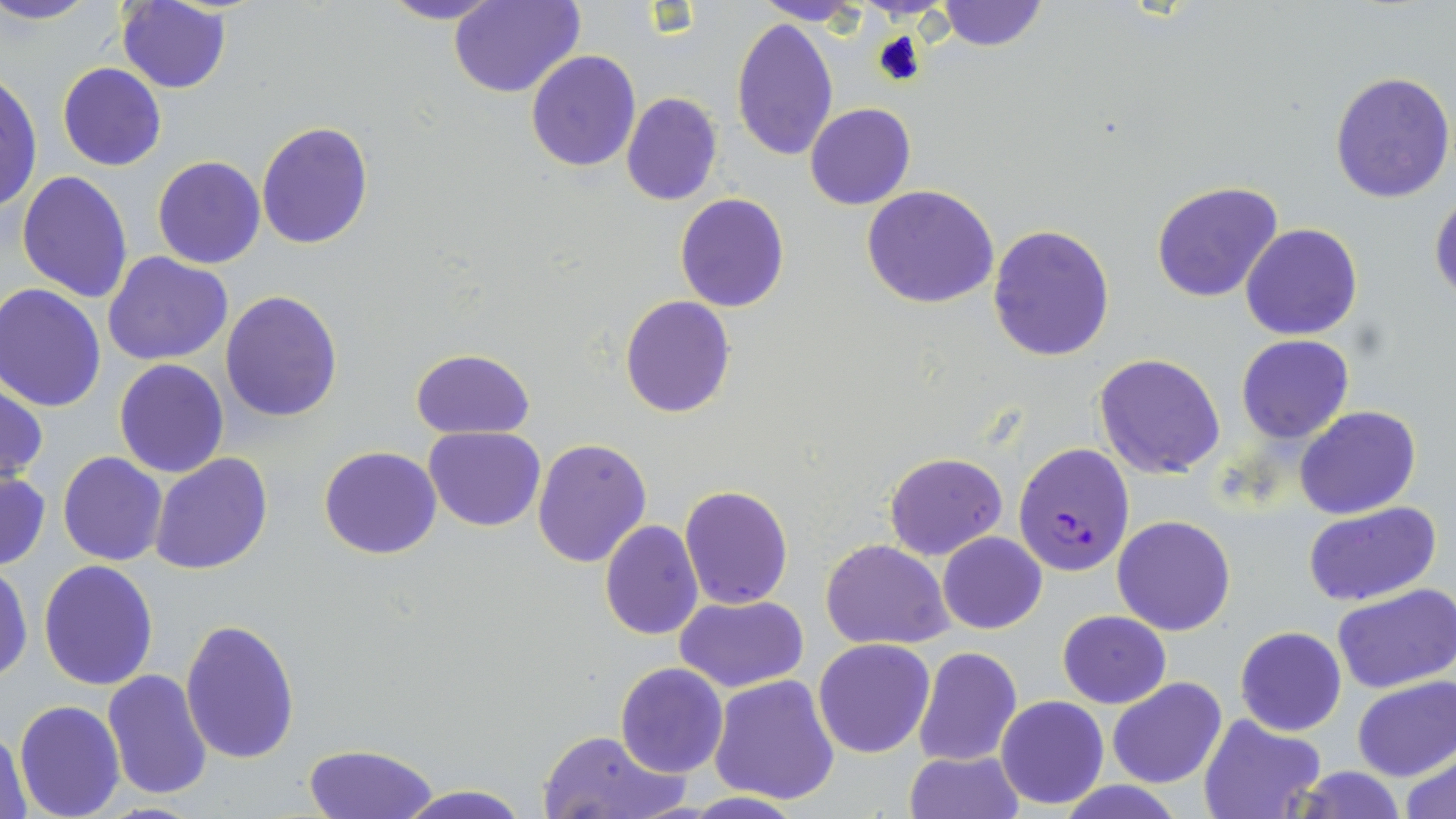

{
  "slide_level_diagnosis": "Plasmodium falciparum",
  "magnification": "1000x",
  "uninfected_red_blood_cell_locations": "approximate bounding boxes as (x1,y1)-(x2,y2) corner pairs in pixels: (0,0)-(102,26), (378,0)-(510,25), (754,0)-(867,26), (935,0)-(1048,52), (117,1)-(232,94), (448,1)-(584,99), (731,16)-(840,161), (526,48)-(640,172), (56,62)-(167,171), (1330,70)-(1455,204), (0,72)-(42,216), (620,93)-(723,206), (804,103)-(916,210), (256,121)-(374,249), (153,155)-(266,269), (17,169)-(133,304), (1151,179)-(1283,304), (861,184)-(1000,309), (1429,188)-(1456,302), (675,192)-(789,311), (1241,223)-(1363,340), (987,224)-(1115,363), (104,252)-(233,365), (0,285)-(107,411), (221,291)-(343,423), (620,296)-(735,419), (1236,334)-(1354,444), (410,347)-(534,440), (1093,353)-(1226,477), (114,359)-(229,477), (0,382)-(46,489), (1293,406)-(1421,519), (424,426)-(545,530), (532,439)-(652,569), (319,445)-(442,560), (58,451)-(167,566), (883,451)-(1007,560), (151,453)-(272,575), (0,471)-(50,570), (679,484)-(794,610), (1303,501)-(1442,604), (1112,515)-(1236,635), (598,518)-(704,640), (938,532)-(1046,634), (821,538)-(953,650), (0,556)-(33,684), (39,560)-(159,690), (1331,584)-(1456,694), (675,594)-(808,691), (1058,609)-(1171,709), (182,619)-(301,764), (1235,626)-(1347,736), (812,638)-(936,759), (914,647)-(1021,766), (615,662)-(729,778), (102,670)-(212,798), (709,674)-(841,806), (1107,676)-(1228,789), (1353,677)-(1455,782), (995,695)-(1108,810), (13,699)-(125,818), (1197,712)-(1328,819), (0,727)-(31,816), (536,729)-(687,818), (301,743)-(438,818), (1401,746)-(1456,818), (903,750)-(1022,819), (1291,766)-(1410,819), (395,783)-(531,819), (680,792)-(809,818)",
  "stain": "May-Grünwald-Giemsa",
  "modality": "light microscopy",
  "plasmodium_falciparum_infected_red_blood_cell_locations": "approximate bounding boxes as (x1,y1)-(x2,y2) corner pairs in pixels: (1017,444)-(1136,577)",
  "image_size": "1456×819 pixels",
  "field_of_view": "one of a larger specimen",
  "preparation": "thin blood smear"
}